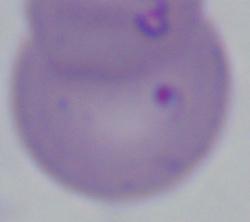
magnification = 1000x
identification = Babesia
modality = micrograph